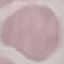
malaria status = uninfected
stain = Giemsa
image type = automatically extracted cell patch, resized to 64 × 64 pixels
preparation = thin blood film
capture = smartphone camera at the microscope eyepiece